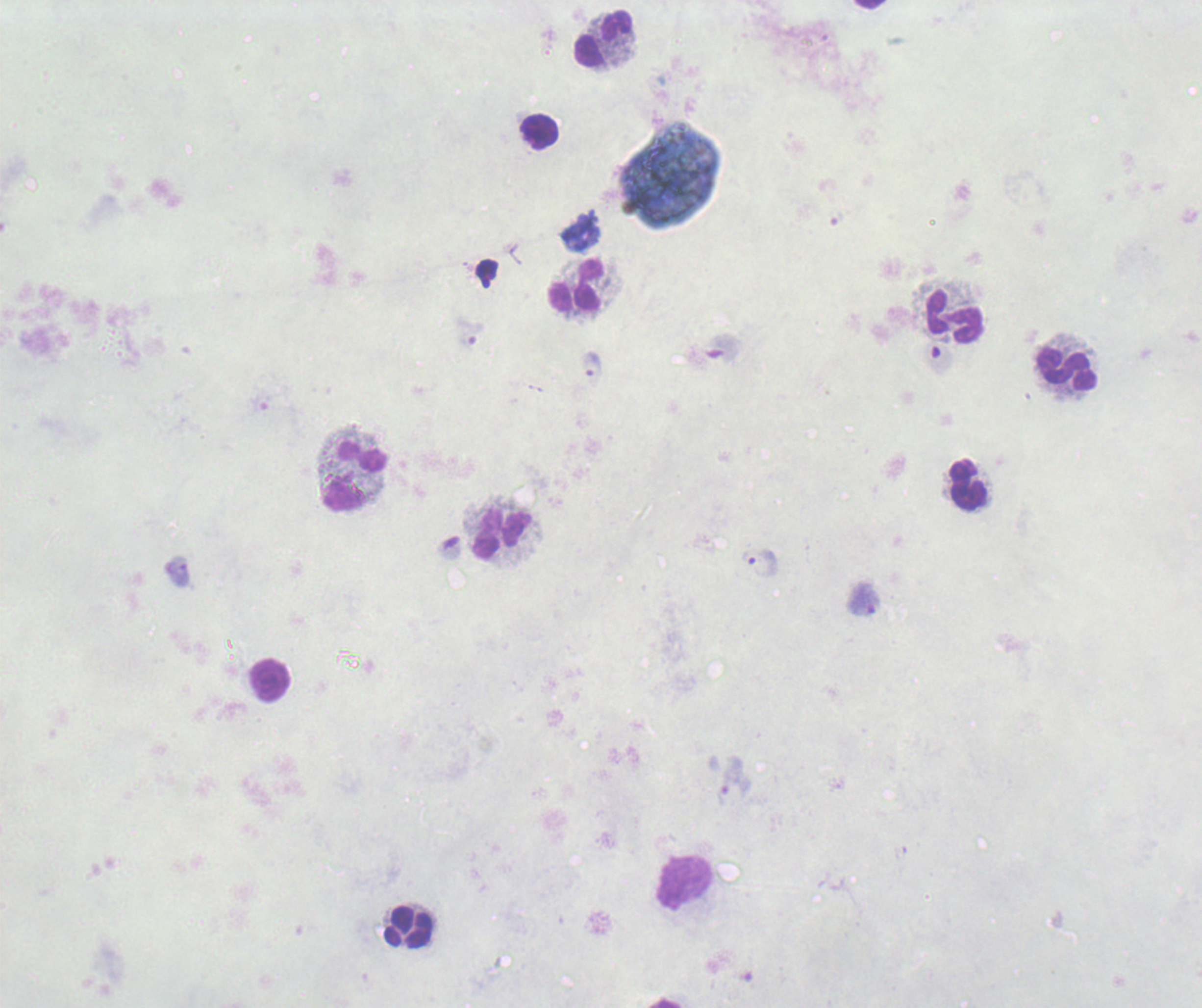
Approximate object centers, in pixels from the top-left corner.
Summary:
  - Leukocyte locations: (x=603, y=38), (x=540, y=132), (x=577, y=286), (x=954, y=317), (x=1067, y=370), (x=356, y=476), (x=967, y=484), (x=502, y=534), (x=270, y=681), (x=685, y=882), (x=408, y=928)
  - Trophozoite locations: (x=592, y=367), (x=759, y=563), (x=177, y=572)
  - Preparation: thick smear of blood
  - Background quality: unsatisfactory
  - Result: malaria parasites identified
  - Context: previously used in a real diagnosis
  - Image size: 1202×1008 pixels
  - Magnification: 100x
  - Field of view: single
  - Stain: Romanowsky